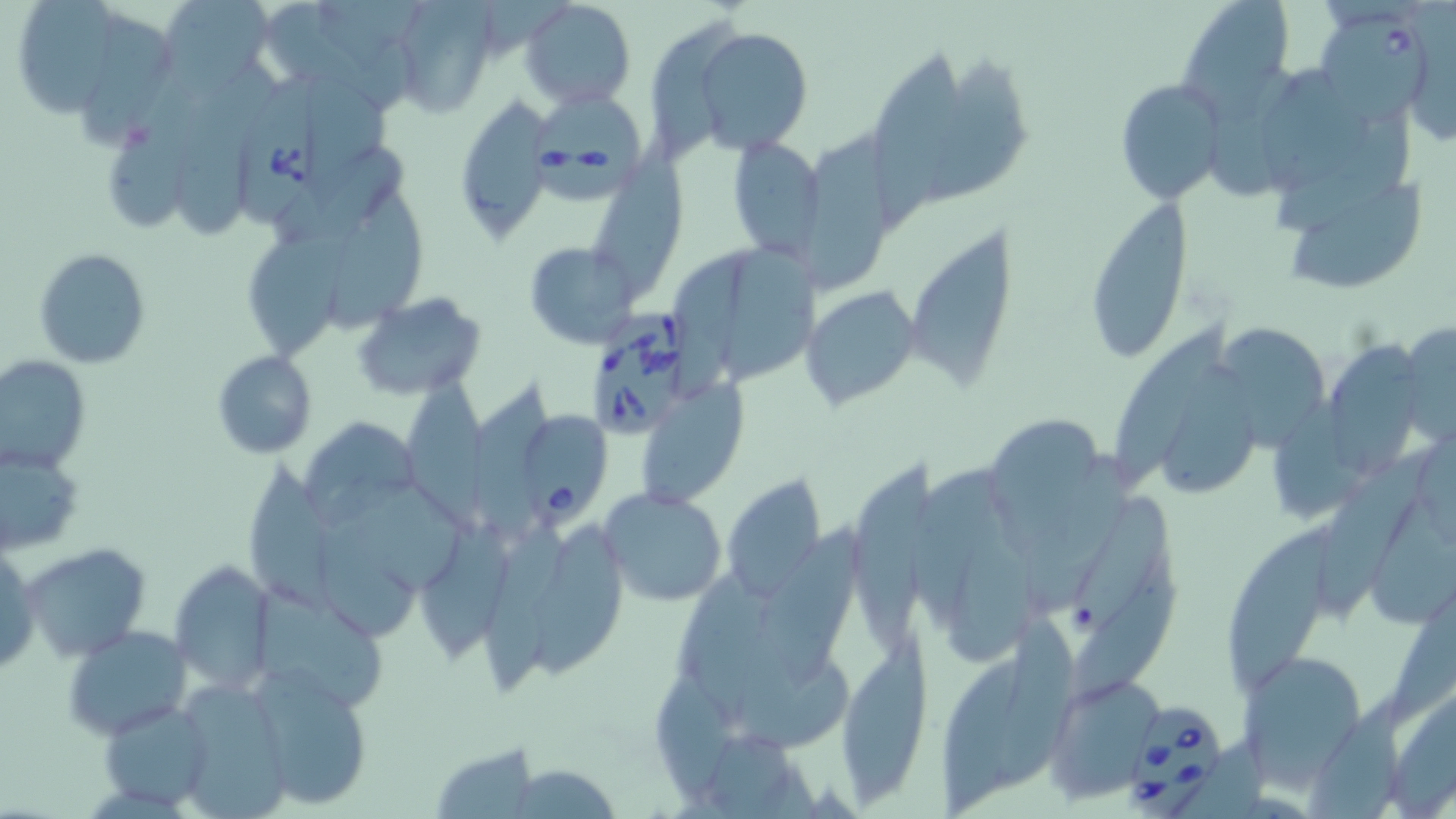
slide-level diagnosis = Babesia divergens
uninfected red blood cell locations = approximate bounding boxes as (x1, y1, x2, y2) in pixels: (19, 0, 120, 119), (520, 0, 635, 110), (1176, 0, 1295, 113), (170, 1, 272, 100), (389, 1, 496, 117), (264, 4, 417, 108), (87, 8, 166, 148), (653, 15, 750, 165), (694, 26, 813, 155), (869, 52, 963, 222), (923, 53, 1034, 205), (178, 63, 283, 246), (1211, 64, 1314, 202), (1270, 65, 1364, 194), (112, 76, 205, 233), (308, 77, 395, 185), (1114, 78, 1228, 204), (453, 97, 554, 243), (1276, 114, 1418, 233), (797, 128, 902, 290), (596, 136, 689, 305), (727, 136, 826, 262), (276, 146, 408, 242), (1287, 183, 1429, 291), (328, 184, 436, 333), (1081, 198, 1191, 363), (907, 225, 1023, 387), (238, 228, 349, 363), (521, 240, 642, 349), (729, 240, 830, 378), (35, 248, 153, 369), (675, 250, 759, 407), (803, 286, 920, 409), (353, 291, 488, 402), (1121, 319, 1231, 479), (1215, 321, 1326, 446), (1397, 325, 1456, 439), (1330, 334, 1427, 479), (213, 350, 317, 458), (0, 354, 89, 472), (1161, 356, 1267, 496), (406, 378, 489, 544), (637, 383, 751, 508), (476, 387, 552, 544), (1278, 391, 1368, 521), (299, 416, 419, 524), (992, 418, 1105, 557), (1320, 441, 1445, 614), (0, 444, 85, 556), (1322, 446, 1436, 620), (1038, 450, 1139, 607), (842, 452, 942, 651), (236, 453, 337, 617), (908, 466, 1004, 635), (719, 473, 828, 599), (1373, 485, 1456, 629), (598, 486, 728, 606), (341, 488, 471, 592), (1071, 491, 1169, 636), (417, 513, 515, 662), (1220, 518, 1346, 690), (318, 522, 416, 641), (763, 523, 861, 686), (528, 524, 630, 685), (958, 537, 1039, 666), (24, 543, 153, 663), (0, 546, 39, 678), (170, 561, 276, 696), (1072, 561, 1178, 701), (681, 565, 773, 729), (256, 581, 393, 702), (1392, 598, 1456, 717), (990, 614, 1077, 798), (64, 625, 192, 738), (836, 646, 933, 800), (938, 648, 1042, 816), (1238, 651, 1364, 785), (741, 659, 858, 756), (252, 667, 376, 812), (1044, 675, 1164, 799), (185, 679, 286, 819), (97, 698, 215, 809), (1308, 700, 1414, 819), (430, 739, 541, 817)
field of view = one of a larger specimen
magnification = 1000x
image size = 1456×819 pixels
Babesia divergens-infected red blood cell locations = approximate bounding boxes as (x1, y1, x2, y2) in pixels: (1316, 10, 1434, 129), (243, 73, 323, 228), (534, 93, 650, 200), (581, 311, 706, 440), (520, 410, 615, 528), (1132, 698, 1219, 815)
modality = optical microscopy
stain = May-Grünwald-Giemsa
preparation = thin blood smear